Comment on the morphology of the erythrocytes.
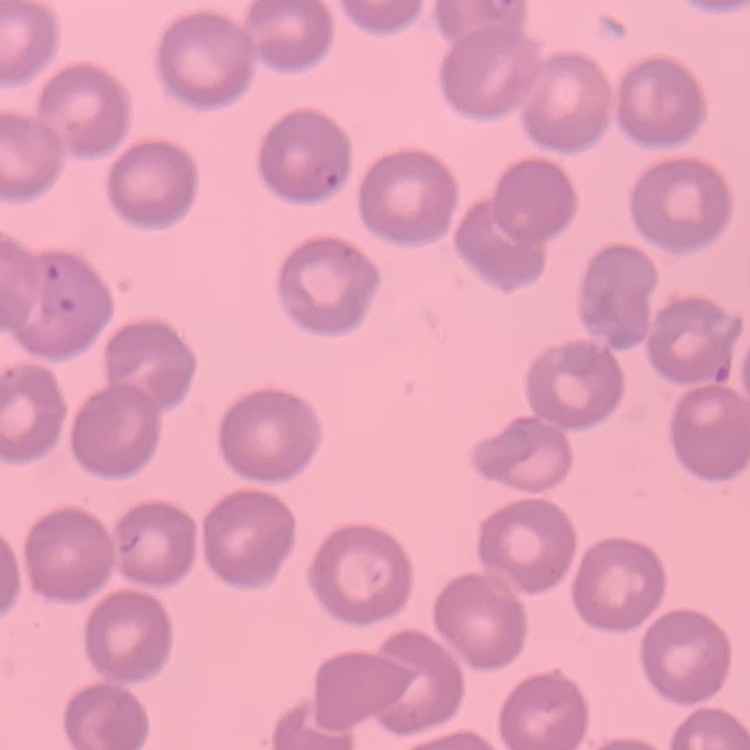

No rouleaux formation.

Summary:
  - Preparation: thin peripheral smear
  - Stain: Field's or Giemsa
  - Image type: square crop of a larger photomicrograph